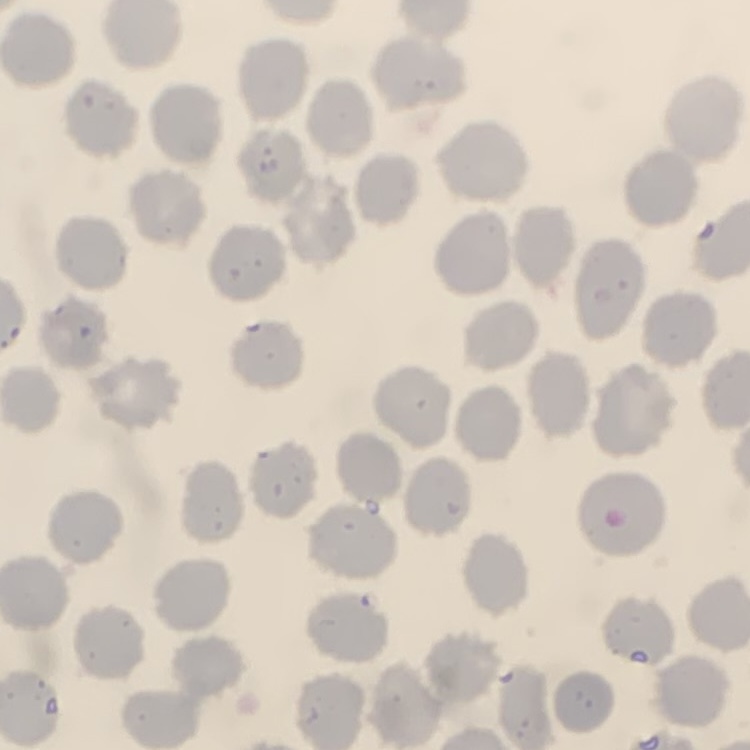

red_blood_cell_morphology: no rouleaux formation
image_type: one tile cut from a larger photomicrograph
preparation: thin blood film
stain: Field's or Giemsa